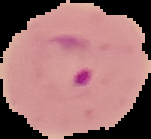

preparation: thin blood smear
image_size: 151×139 pixels
result: Plasmodium parasites identified
image_type: segmented cell region on a black background